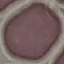
Summary:
  - Malaria status: uninfected
  - Preparation: thin smear
  - Image type: automatically extracted cell patch, resized to 64 × 64 pixels
  - Capture: smartphone camera at the microscope eyepiece
  - Stain: Giemsa